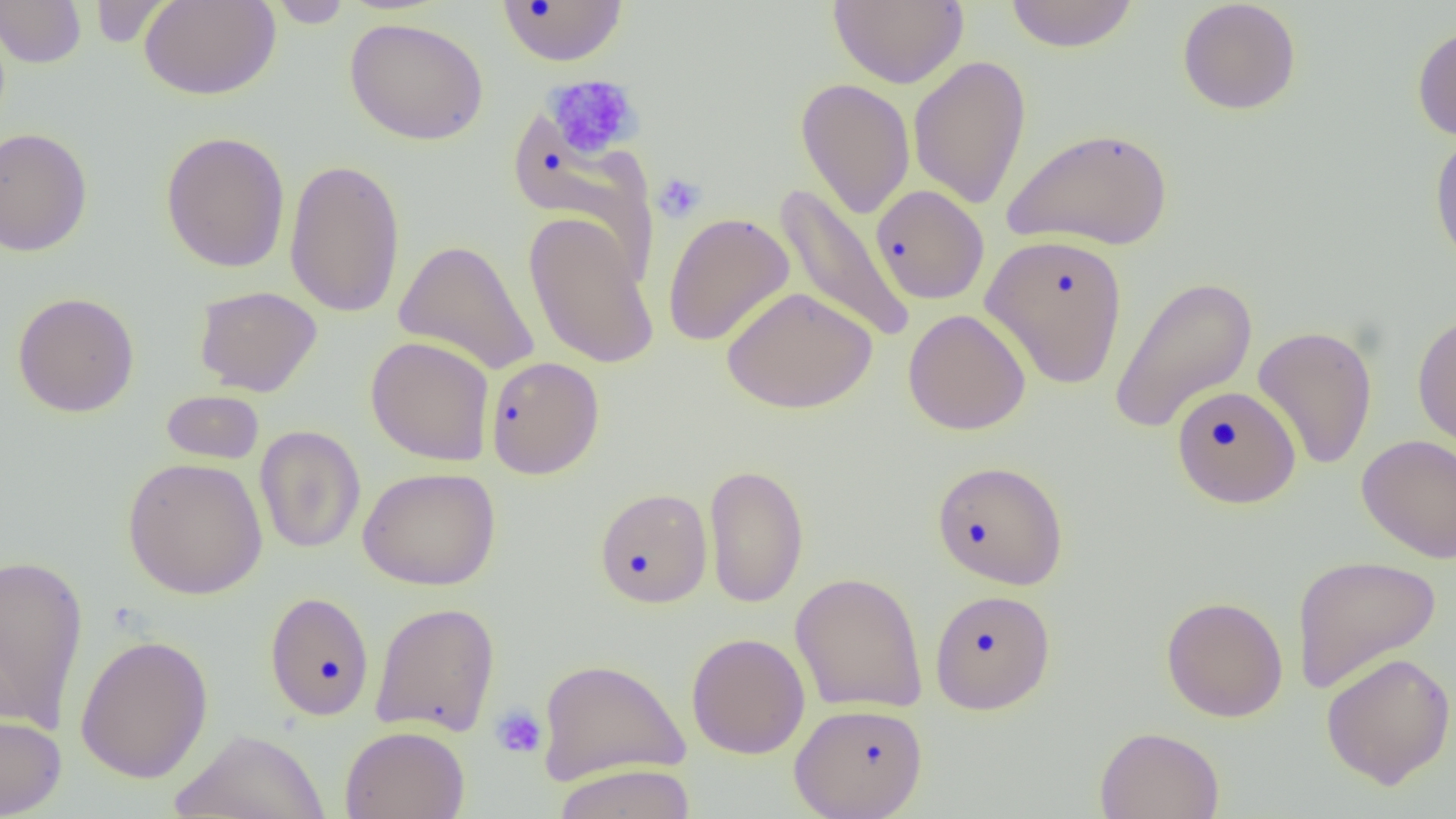
slide-level diagnosis = negative for blood parasites
platelet locations = approximate bounding boxes as (x1,y1)-(x2,y2) corner pairs in pixels: (544,74)-(642,159), (652,172)-(707,224), (490,704)-(548,759)
preparation = thin blood film
uninfected red blood cell locations = approximate bounding boxes as (x1,y1)-(x2,y2) corner pairs in pixels: (139,0)-(281,101), (829,0)-(968,88), (1003,0)-(1140,52), (1177,0)-(1302,115), (0,1)-(86,68), (87,1)-(174,48), (265,1)-(355,28), (496,1)-(629,66), (344,16)-(489,145), (1412,24)-(1456,142), (908,55)-(1031,209), (795,78)-(915,219), (508,110)-(659,287), (1002,126)-(1173,251), (0,127)-(93,256), (1429,129)-(1456,267), (160,131)-(291,273), (284,157)-(406,319), (775,183)-(913,345), (871,185)-(989,305), (523,212)-(660,370), (663,212)-(795,347), (980,233)-(1128,389), (394,239)-(539,376), (1108,275)-(1258,434), (194,285)-(322,397), (722,285)-(877,414), (12,292)-(140,417), (903,308)-(1032,435), (1412,310)-(1456,452), (1252,324)-(1378,471), (366,336)-(495,466), (487,356)-(605,479), (1171,385)-(1302,507), (161,389)-(264,464), (254,425)-(366,554), (1356,433)-(1456,563), (122,457)-(268,600), (931,460)-(1069,590), (703,462)-(809,609), (357,467)-(501,591), (594,486)-(713,608), (0,553)-(89,732), (1291,554)-(1441,694), (790,571)-(928,714), (929,589)-(1056,714), (265,591)-(375,721), (1160,595)-(1289,723), (370,600)-(501,737), (686,632)-(810,759), (74,633)-(214,784), (1320,651)-(1456,789), (536,657)-(691,786), (790,702)-(929,818), (0,710)-(66,818), (340,725)-(470,819), (1094,726)-(1225,819), (171,728)-(330,818), (551,762)-(697,819)
image size = 1456×819 pixels
field of view = one of a larger specimen
modality = optical microscopy
magnification = 1000x